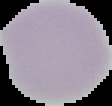
Result: no Plasmodium parasites seen. Image is 112×106 pixels. The area outside the segmented cell region is set to black. From a thin blood smear.